Name the blood parasite species.
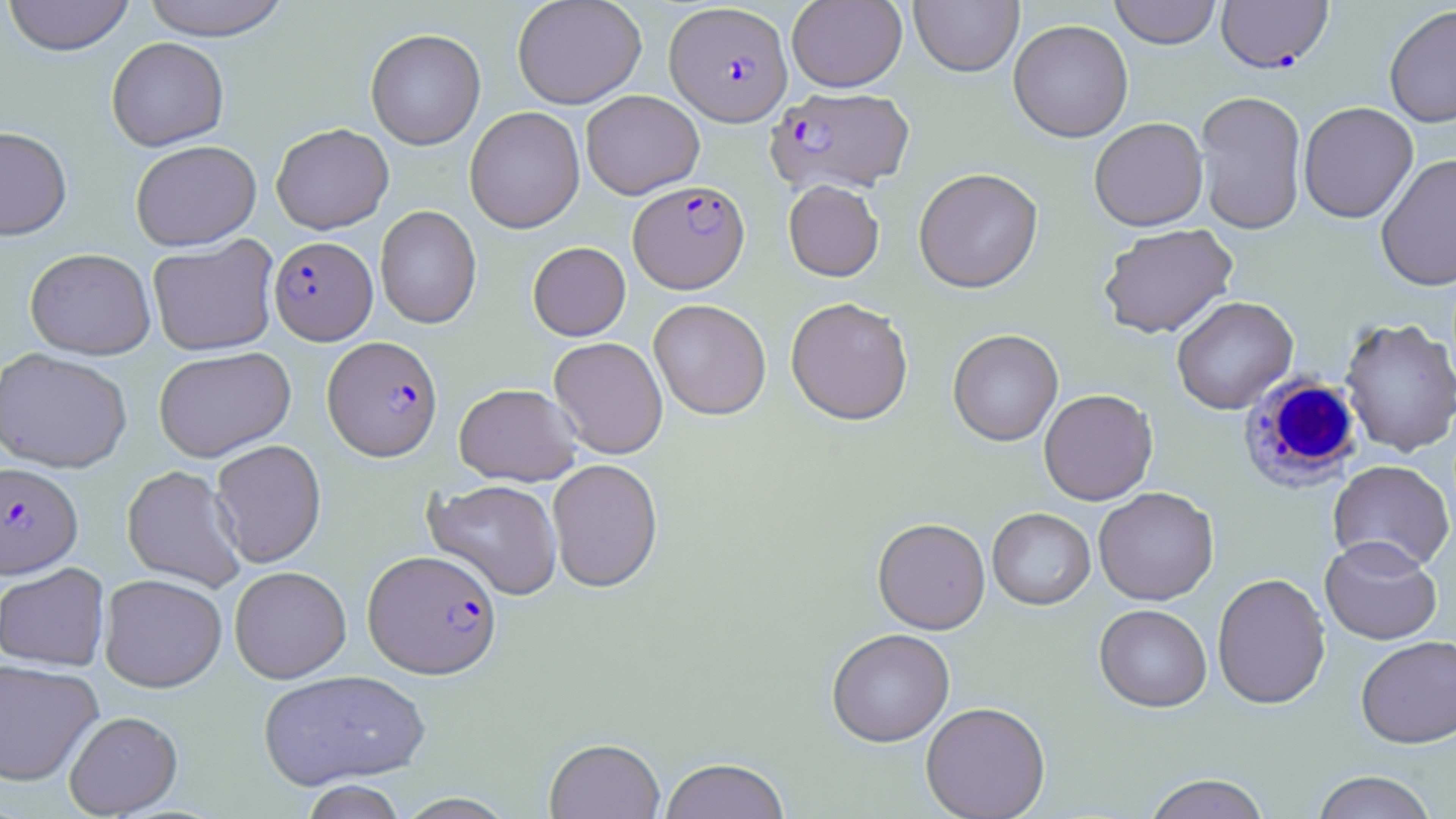
Plasmodium falciparum.

Summary:
  - Coordinate format: approximate bounding boxes as [x1, y1, x2, y2] in pixels
  - Plasmodium falciparum-infected red blood cell locations: [1215, 1, 1333, 73], [664, 3, 792, 126], [766, 86, 915, 194], [628, 180, 749, 294], [269, 236, 377, 345], [322, 335, 443, 461], [0, 462, 83, 578], [362, 549, 502, 679]
  - Uninfected red blood cell locations: [2, 0, 135, 56], [140, 0, 292, 40], [512, 0, 647, 109], [1109, 0, 1221, 49], [787, 1, 907, 92], [909, 1, 1024, 77], [1384, 5, 1456, 128], [1008, 19, 1133, 143], [365, 28, 486, 150], [106, 37, 229, 151], [581, 90, 705, 199], [1194, 90, 1308, 235], [1298, 101, 1418, 224], [465, 106, 585, 233], [1088, 117, 1209, 232], [271, 123, 394, 234], [0, 126, 72, 240], [130, 139, 262, 251], [1375, 153, 1456, 291], [913, 167, 1043, 293], [783, 180, 884, 281], [375, 205, 482, 329], [1098, 223, 1239, 339], [147, 236, 280, 356], [528, 241, 631, 341], [25, 248, 156, 359], [1171, 295, 1298, 415], [785, 297, 913, 426], [648, 298, 771, 420], [1339, 317, 1456, 457], [948, 328, 1063, 446], [548, 336, 668, 459], [153, 346, 296, 462], [0, 348, 132, 473], [454, 382, 582, 486], [1038, 388, 1158, 505], [210, 439, 327, 568], [547, 458, 663, 593], [1327, 459, 1455, 573], [122, 465, 246, 592], [424, 479, 563, 600], [1093, 487, 1219, 605], [987, 507, 1095, 610], [872, 518, 991, 635], [1320, 536, 1442, 645], [0, 563, 110, 671], [229, 566, 351, 683], [1211, 572, 1331, 710], [99, 573, 228, 692], [1094, 603, 1212, 712], [826, 628, 955, 747], [1356, 635, 1456, 747], [0, 659, 103, 787], [257, 669, 430, 790], [920, 701, 1050, 819], [64, 710, 183, 818], [544, 737, 665, 819], [658, 758, 790, 819], [1310, 770, 1439, 819], [1141, 773, 1272, 819], [300, 780, 407, 819], [394, 792, 518, 819]
  - White blood cell locations: [1239, 374, 1365, 490]
  - Preparation: thin blood smear
  - Modality: optical microscopy
  - Image size: 1456×819 pixels
  - Magnification: 1000x
  - Stain: May-Grünwald-Giemsa
  - Field of view: single